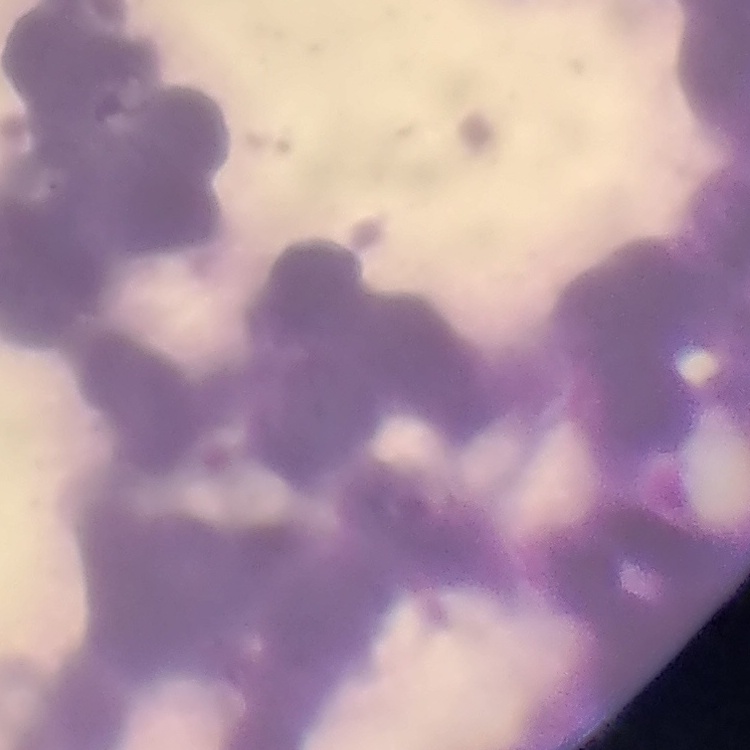

red blood cell morphology = rouleaux formation
image type = one tile cut from a larger photomicrograph
preparation = thin blood smear
stain = Field's or Giemsa